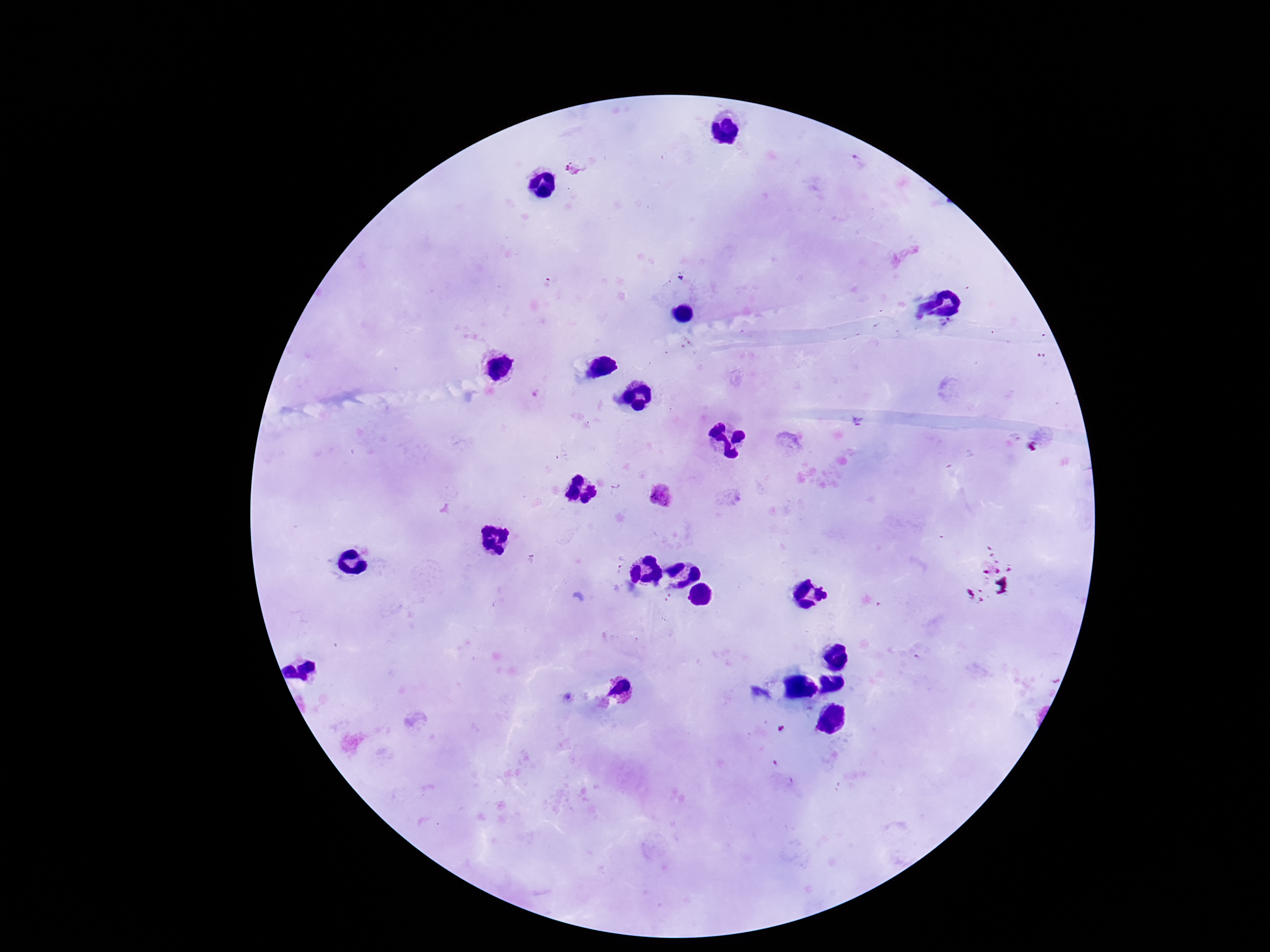 Approximate centers as (x, y) in pixels. Plasmodium parasite locations: (662, 496), (618, 570). Giemsa-stained preparation. Single field of view. Smartphone photograph taken through the microscope eyepiece. 100x magnification. Patient malaria status: positive. Image is 1270×952 pixels. Thick blood smear.